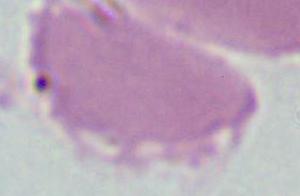
Micrograph. An erythrocyte is shown. Captured at 1000x magnification.